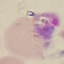
Malaria status: uninfected. Thin smear of blood. Giemsa-stained preparation. Photographed with a smartphone camera at the microscope eyepiece. Automatically extracted cell patch, resized to 64 × 64 pixels.